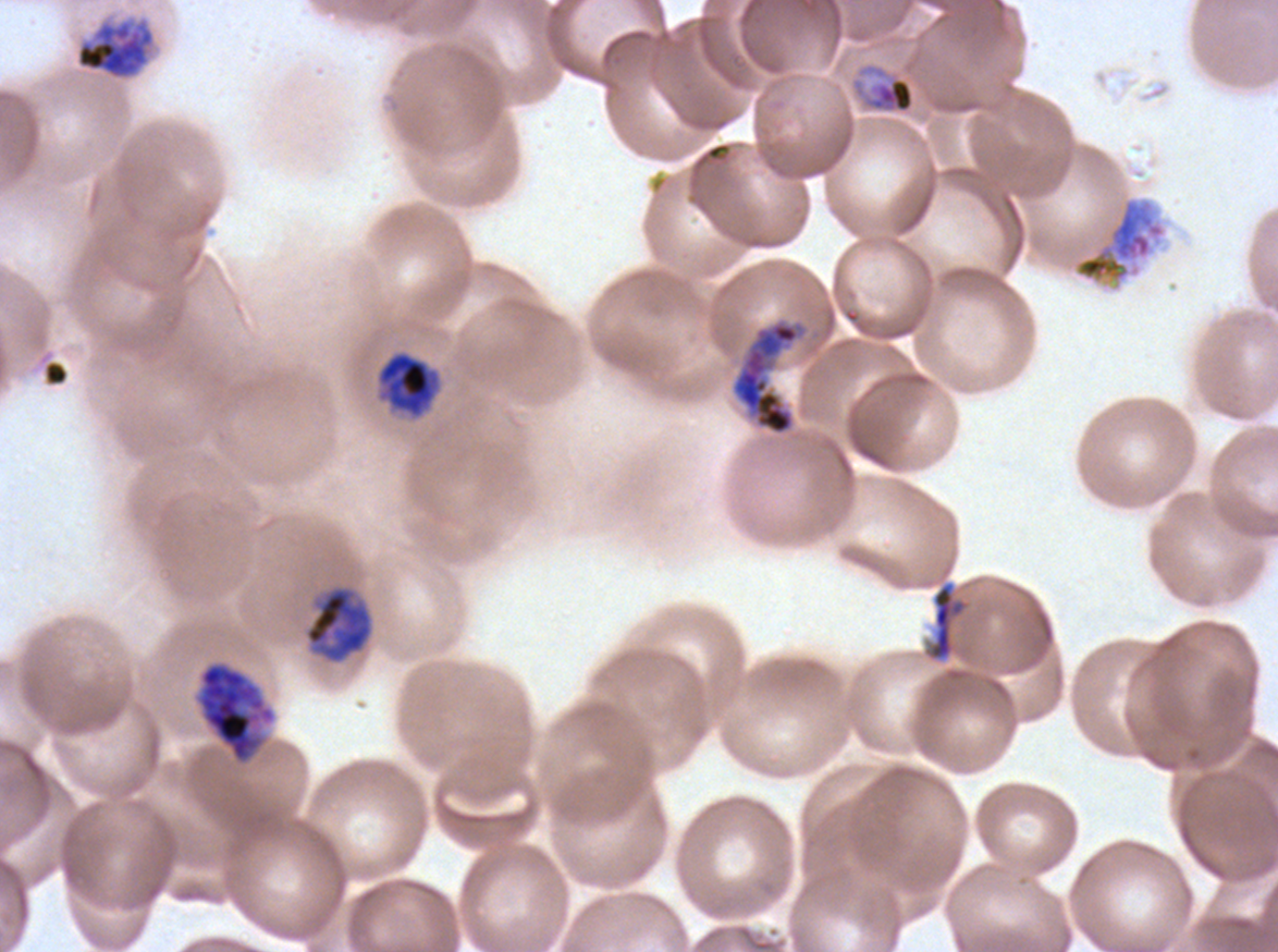
Approximate bounding boxes as (x1, y1, x2, y2) in pixels. Early schizont locations: (75, 15, 156, 81), (731, 320, 804, 435), (375, 350, 441, 419), (304, 587, 372, 663), (196, 662, 276, 764). Debris locations: (44, 361, 68, 384), (925, 581, 969, 662). Late schizont locations: (1073, 197, 1166, 286). Mid trophozoite locations: (850, 62, 915, 115). Thin blood film. Image is 1278×952 pixels. Giemsa-stained preparation. Life-cycle stages observed: mid trophozoite, early schizont, late schizont. A sub-image separated from a larger composite. P. falciparum cultured ex vivo for 24 to 48 hours, from a patient in The Gambia.